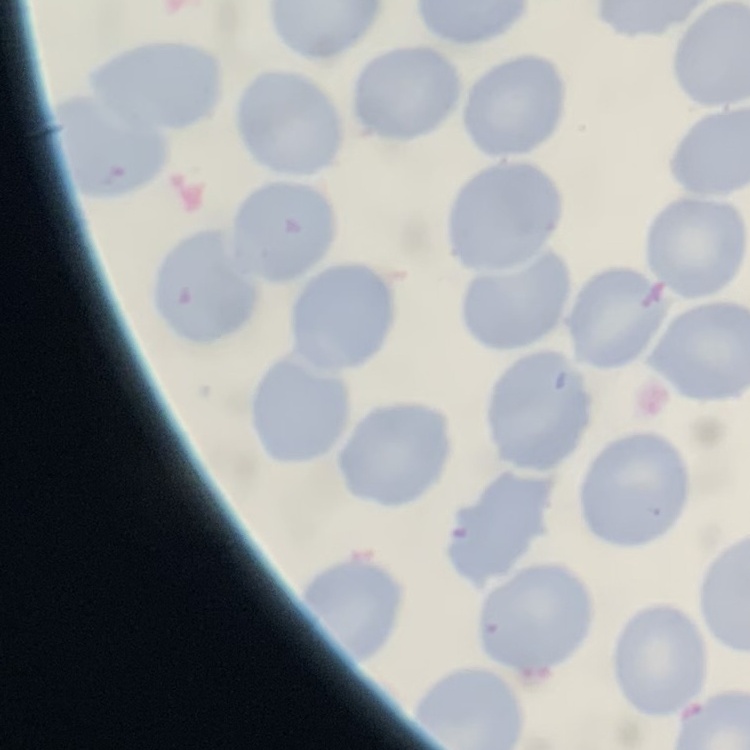
The red blood cells exhibit no rouleaux formation. Stained with either Field's or Giemsa. Square crop of a larger photomicrograph. Thin blood smear.